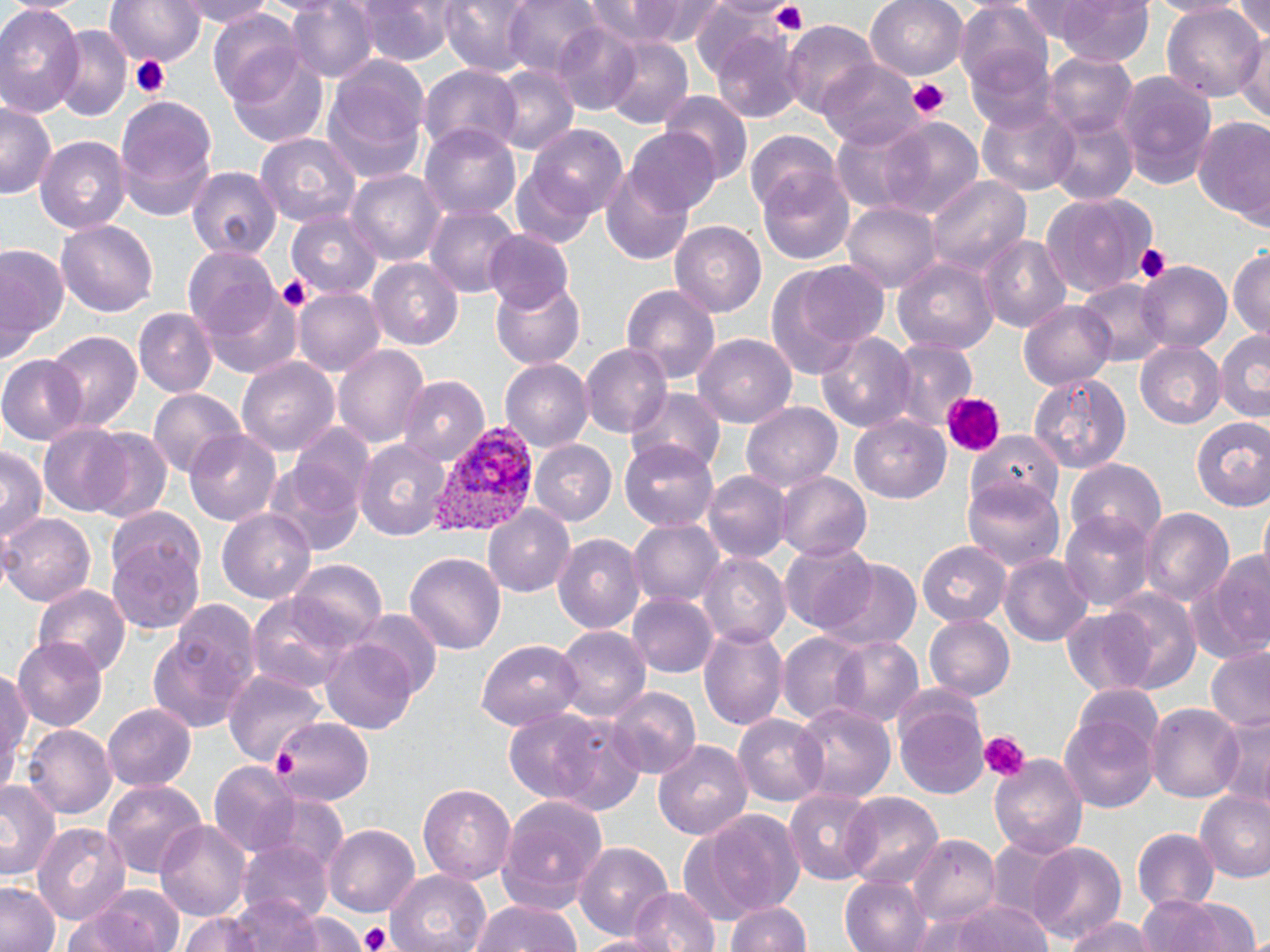
plasmodium_vivax_infected_red_blood_cell_locations: 'approximate bounding boxes as [x1, y1, x2, y2] in pixels: [428, 423, 535, 535]'
slide_level_diagnosis: Plasmodium vivax
preparation: thin blood smear
image_size: 1270×952 pixels
platelet_locations: 'approximate bounding boxes as [x1, y1, x2, y2] in pixels: [767, 2, 811, 36], [129, 53, 169, 99], [907, 78, 951, 121], [1131, 241, 1172, 285], [275, 273, 312, 311], [940, 392, 1006, 455], [979, 730, 1030, 780], [272, 746, 298, 779], [358, 924, 394, 951]'
field_of_view: one of a larger specimen
uninfected_red_blood_cell_locations: 'approximate bounding boxes as [x1, y1, x2, y2] in pixels: [106, 0, 202, 67], [177, 0, 278, 26], [346, 0, 458, 65], [440, 0, 535, 73], [504, 0, 604, 77], [582, 0, 726, 48], [866, 0, 968, 79], [1050, 0, 1154, 67], [1225, 0, 1270, 44], [286, 1, 374, 83], [689, 2, 789, 81], [956, 3, 1055, 99], [1162, 4, 1267, 104], [0, 5, 84, 117], [208, 12, 306, 104], [784, 22, 882, 119], [550, 24, 644, 114], [51, 26, 131, 122], [711, 27, 802, 120], [1238, 29, 1270, 122], [599, 35, 692, 128], [962, 43, 1058, 136], [229, 53, 328, 147], [332, 53, 431, 143], [1044, 53, 1134, 140], [819, 61, 921, 150], [490, 64, 579, 154], [420, 65, 522, 153], [1114, 70, 1219, 192], [322, 86, 425, 185], [662, 94, 752, 185], [114, 97, 217, 219], [0, 101, 56, 199], [978, 101, 1079, 195], [1044, 110, 1137, 206], [874, 116, 983, 216], [1194, 117, 1270, 229], [832, 122, 936, 217], [421, 124, 523, 222], [531, 128, 628, 217], [626, 128, 722, 217], [746, 131, 839, 216], [254, 133, 361, 230], [35, 136, 130, 232], [600, 163, 693, 268], [189, 164, 279, 261], [757, 168, 857, 265], [348, 169, 444, 265], [510, 170, 592, 252], [927, 174, 1031, 274], [1041, 191, 1155, 295], [843, 202, 939, 293], [426, 205, 521, 298], [286, 209, 383, 299], [57, 221, 157, 315], [671, 222, 766, 317], [484, 230, 575, 311], [978, 234, 1072, 333], [0, 243, 66, 361], [183, 249, 282, 343], [1228, 250, 1270, 342], [767, 256, 886, 374], [891, 256, 999, 355], [370, 260, 462, 349], [1136, 261, 1231, 355], [492, 277, 588, 369], [1076, 278, 1167, 365], [621, 282, 721, 384], [294, 286, 384, 376], [200, 287, 301, 379], [1020, 300, 1114, 390], [135, 308, 216, 397], [1216, 327, 1270, 422], [45, 328, 142, 432], [816, 332, 916, 432], [695, 334, 798, 428], [888, 340, 977, 431], [1137, 341, 1226, 426], [581, 343, 672, 440], [334, 344, 428, 449], [0, 355, 87, 442], [238, 357, 338, 458], [501, 360, 592, 452], [1027, 373, 1134, 475], [400, 377, 489, 467], [628, 388, 725, 471], [147, 389, 247, 482], [743, 401, 840, 492], [850, 412, 950, 501], [1190, 417, 1270, 512], [37, 423, 136, 517], [288, 425, 374, 515], [86, 428, 172, 523], [967, 428, 1064, 508], [185, 431, 280, 524], [621, 439, 723, 531], [354, 441, 451, 539], [529, 441, 617, 526], [0, 447, 46, 548], [1066, 458, 1167, 548], [262, 460, 365, 559], [706, 471, 789, 563], [776, 473, 872, 562], [961, 475, 1064, 574], [484, 505, 576, 596], [1139, 508, 1232, 608], [217, 510, 314, 602], [1059, 510, 1154, 609], [0, 513, 95, 608], [630, 519, 723, 609], [104, 530, 209, 635], [553, 534, 643, 635], [917, 541, 1010, 625], [780, 542, 874, 633], [1194, 547, 1270, 666], [404, 550, 506, 653], [698, 552, 790, 650], [999, 553, 1091, 648], [290, 557, 387, 645], [816, 560, 920, 652], [31, 582, 130, 678], [1098, 590, 1204, 697], [248, 593, 350, 694], [630, 593, 717, 677], [151, 603, 261, 734], [1060, 609, 1154, 692], [345, 612, 442, 704], [924, 614, 1013, 703], [700, 622, 789, 731], [555, 626, 650, 724], [10, 634, 106, 729], [777, 634, 866, 724], [827, 636, 923, 730], [320, 639, 419, 734], [478, 639, 581, 730], [1206, 648, 1270, 733], [1, 669, 30, 792], [224, 671, 324, 765], [610, 685, 702, 779], [1071, 686, 1166, 766], [103, 702, 197, 790], [792, 703, 894, 806], [1148, 703, 1243, 804], [895, 705, 992, 802], [499, 709, 624, 808], [1219, 711, 1269, 805], [733, 714, 827, 806], [1059, 717, 1158, 812], [272, 718, 373, 806], [25, 725, 116, 819], [652, 739, 753, 840], [989, 752, 1088, 861], [209, 763, 298, 855], [0, 778, 63, 882], [101, 779, 207, 880], [419, 784, 516, 887], [785, 786, 881, 886], [1196, 790, 1270, 884], [841, 792, 944, 889], [265, 793, 350, 876], [495, 795, 609, 914], [703, 809, 807, 920], [154, 820, 250, 923], [33, 822, 130, 924], [324, 824, 420, 919], [1133, 828, 1218, 915], [910, 834, 1002, 929], [986, 837, 1070, 924], [239, 839, 334, 926], [574, 840, 672, 940], [1027, 841, 1128, 944], [386, 869, 489, 952], [838, 874, 930, 952], [0, 882, 62, 952], [85, 885, 187, 952], [627, 885, 721, 952], [199, 896, 331, 952], [1143, 897, 1261, 952], [470, 898, 583, 952], [925, 898, 1055, 952], [726, 899, 815, 952], [178, 911, 262, 951], [298, 914, 364, 952], [1063, 915, 1156, 952], [571, 931, 678, 951]'
magnification: 1000x
modality: light microscopy
stain: May-Grünwald-Giemsa